Assess this cell for malaria.
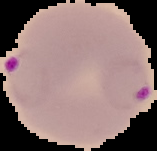
It is parasitized.

Image is 157×151 pixels. The area outside the segmented cell region is set to black. From a thin blood film.